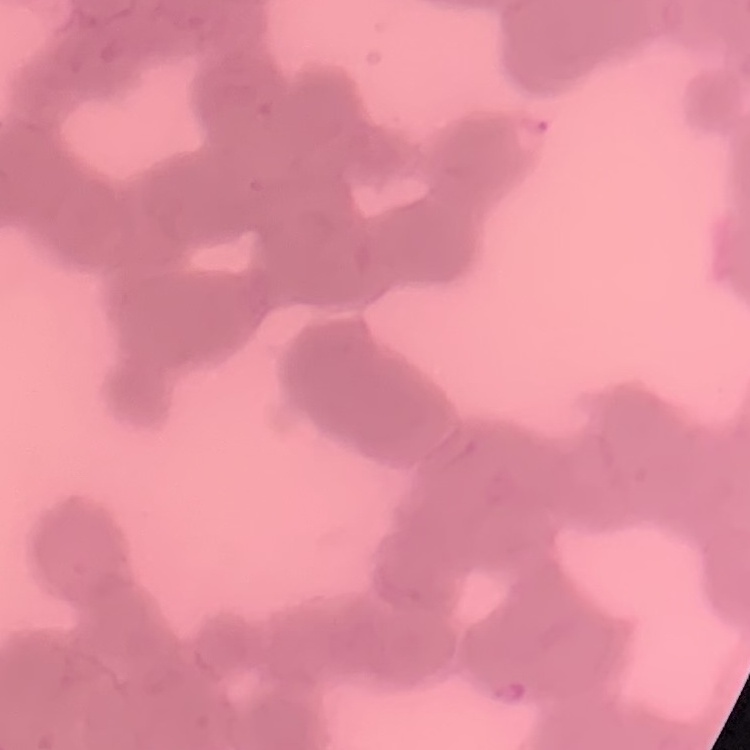 The red blood cells exhibit rouleaux formation. Thin blood film. Stained with either Field's or Giemsa. One tile cut from a larger photomicrograph.